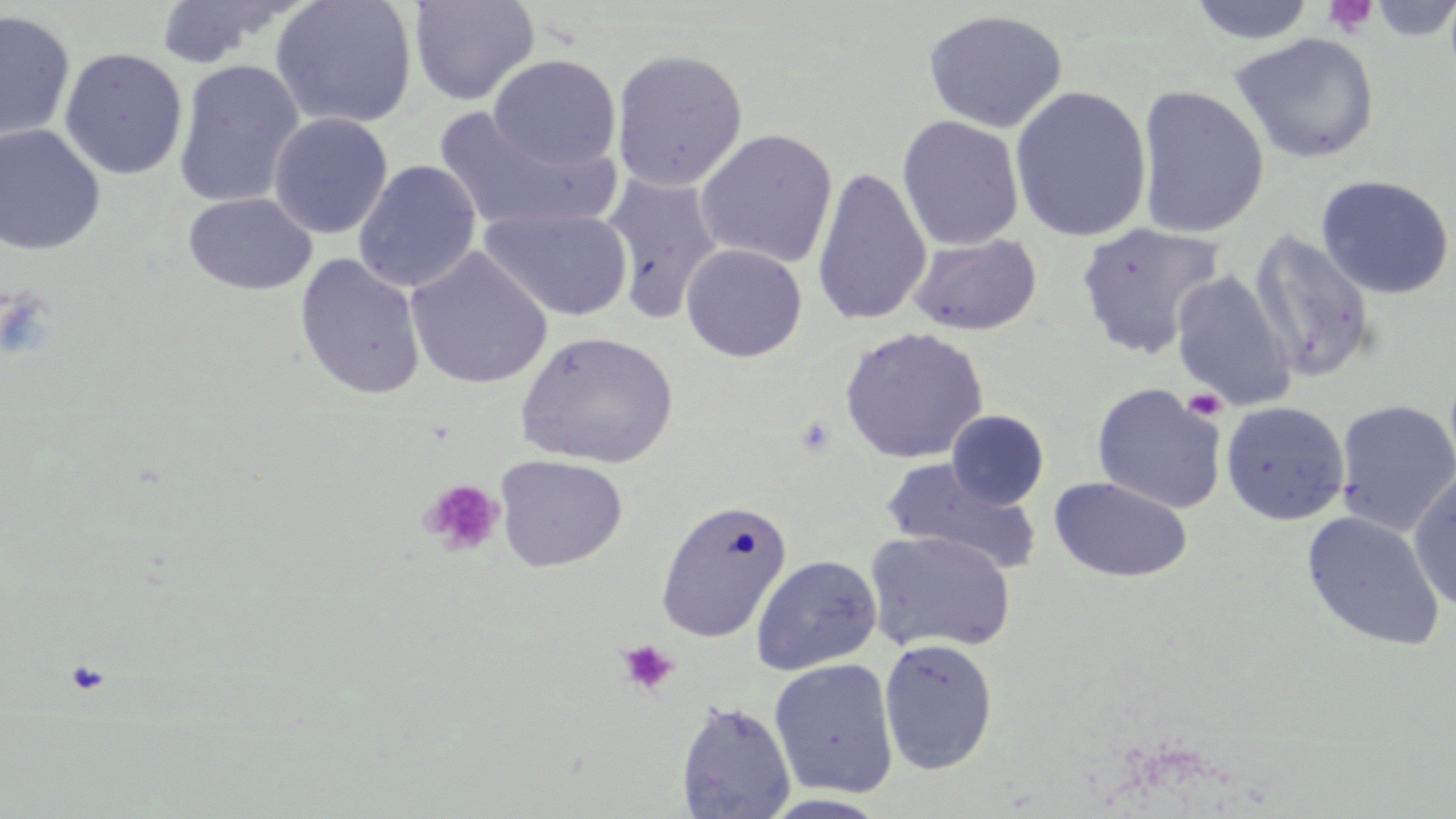
Approximate bounding boxes as (x1, y1, x2, y2) in pixels. Uninfected red blood cell locations: (154, 0, 299, 70), (270, 0, 419, 130), (408, 0, 540, 107), (1365, 0, 1456, 42), (1187, 1, 1317, 45), (922, 9, 1069, 133), (0, 10, 75, 146), (1229, 32, 1380, 164), (59, 48, 188, 180), (610, 48, 748, 193), (488, 54, 621, 172), (172, 59, 305, 209), (1136, 85, 1270, 239), (1009, 86, 1152, 243), (432, 106, 616, 234), (268, 113, 392, 239), (897, 115, 1024, 251), (0, 124, 106, 256), (695, 128, 838, 269), (353, 159, 482, 293), (811, 167, 932, 328), (598, 173, 723, 323), (1316, 174, 1455, 299), (182, 193, 317, 295), (479, 206, 633, 321), (1075, 222, 1224, 359), (1249, 231, 1375, 381), (908, 234, 1042, 336), (680, 243, 807, 362), (405, 247, 552, 390), (294, 254, 427, 401), (1170, 270, 1296, 411), (838, 327, 988, 464), (515, 331, 678, 470), (1091, 383, 1226, 514), (1335, 400, 1456, 536), (1221, 401, 1349, 525), (946, 409, 1049, 510), (494, 454, 628, 572), (881, 459, 1041, 575), (1408, 470, 1456, 612), (1049, 477, 1192, 583), (655, 498, 792, 643), (1301, 511, 1445, 651), (865, 530, 1017, 655), (751, 554, 882, 674), (878, 638, 998, 775), (768, 659, 899, 799), (676, 700, 796, 818). Platelet locations: (1323, 0, 1379, 39), (0, 289, 56, 361), (1182, 388, 1226, 421), (794, 415, 838, 457), (419, 478, 504, 556), (616, 639, 679, 696), (66, 659, 110, 695). Slide-level diagnosis: no evidence of blood parasites. Light microscopy. 1000x magnification. Image is 1456×819 pixels. Single field of view. Thin blood film. May-Grünwald-Giemsa-stained preparation.